Classify this cell by malaria status.
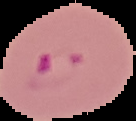
Parasitized.

{
  "image_type": "cell region segmented out of the field of view; surrounding area masked to black",
  "image_size": "136×121 pixels",
  "preparation": "thin blood smear"
}